Identify the parasite.
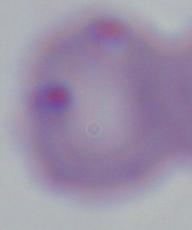
This is Babesia.

magnification: 1000x
modality: micrograph